Assess this cell for malaria.
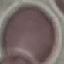
It is uninfected.

{
  "capture": "smartphone camera at the microscope eyepiece",
  "stain": "Giemsa",
  "preparation": "thin blood film",
  "image_type": "automatically extracted cell patch, resized to 64 × 64 pixels"
}